Identify the preparation type.
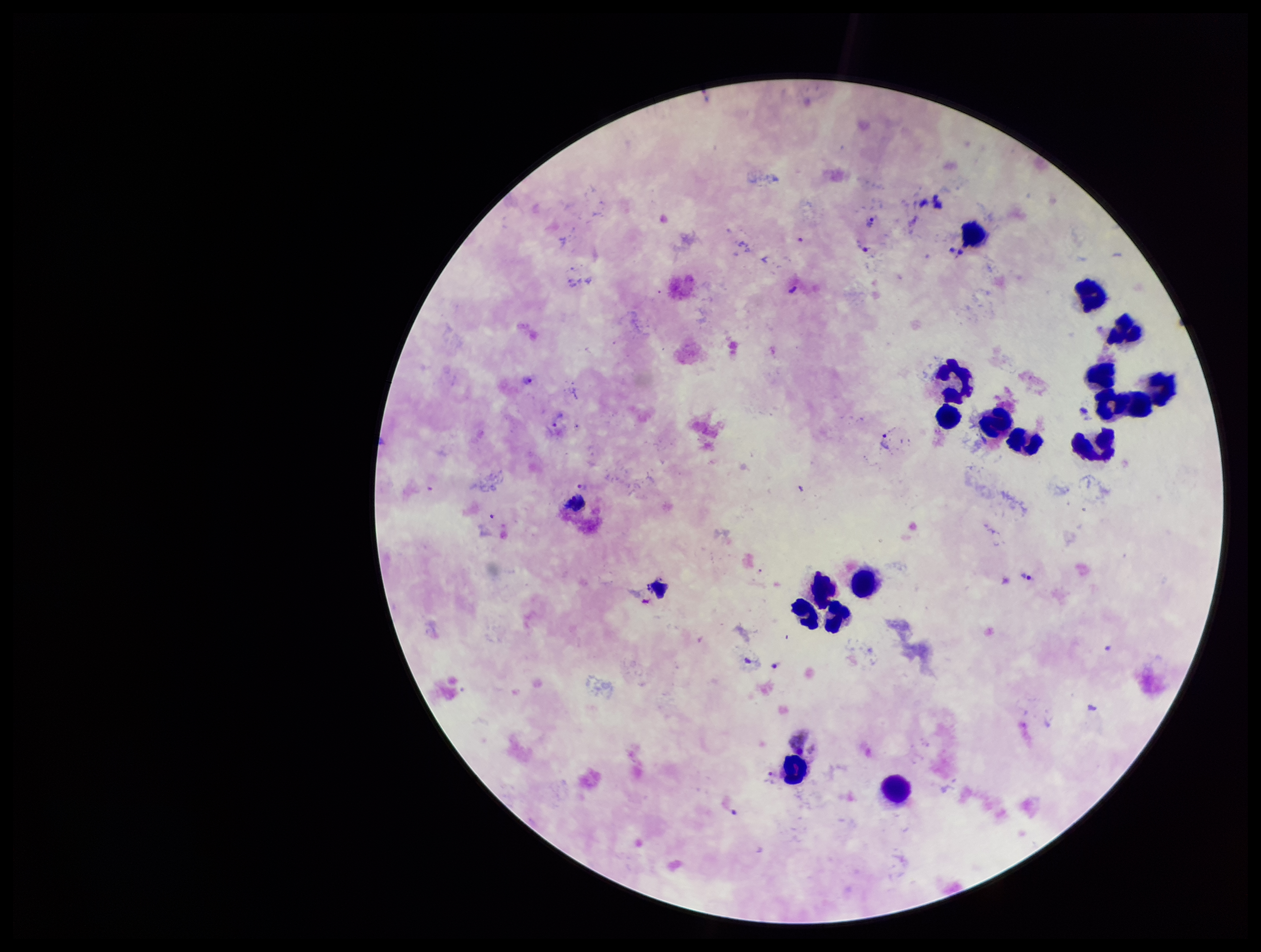

A thick smear.

Patient malaria status: infected. Leukocyte count: 18. Smartphone photograph taken through the eyepiece of a microscope. Giemsa stain. Parasite count: 9. Species reported for this patient: Plasmodium vivax. Image is 1261×952 pixels. One field from this slide. Plasmodium parasites: seen.